Give the extent of all Plasmodium ovale-infected red blood cells.
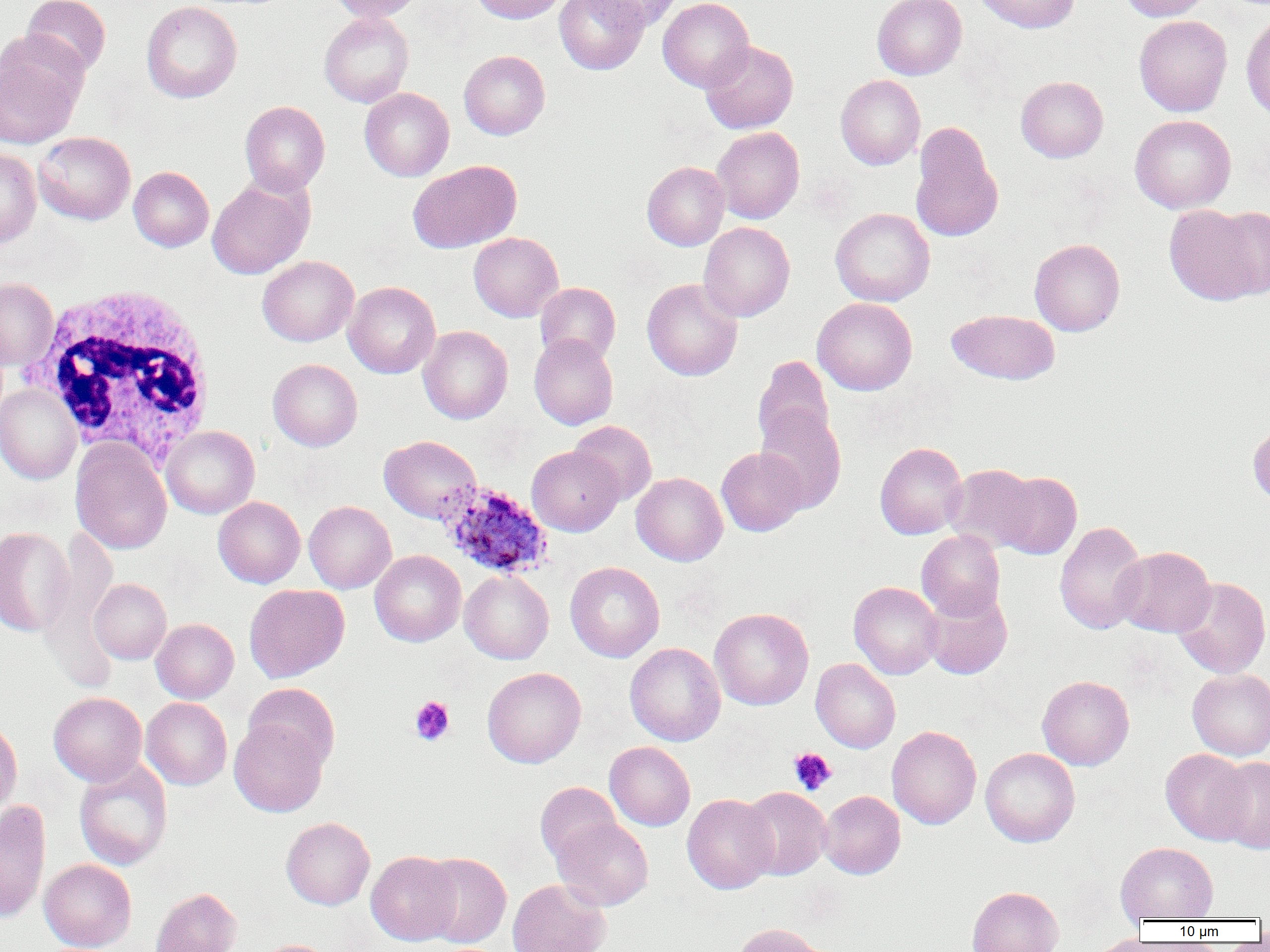

Approximate bounding boxes as named x1/y1/x2/y2 corners in pixels.
Plasmodium ovale-infected red blood cells: (x1=436, y1=482, x2=554, y2=579).

slide_level_diagnosis: Plasmodium ovale
uninfected_red_blood_cell_locations: 'approximate bounding boxes as named x1/y1/x2/y2 corners in pixels: (x1=21, y1=0, x2=111, y2=75), (x1=327, y1=0, x2=425, y2=22), (x1=469, y1=0, x2=566, y2=24), (x1=554, y1=0, x2=649, y2=74), (x1=588, y1=0, x2=682, y2=31), (x1=658, y1=0, x2=754, y2=92), (x1=872, y1=0, x2=966, y2=80), (x1=974, y1=0, x2=1079, y2=33), (x1=1119, y1=0, x2=1213, y2=21), (x1=141, y1=1, x2=242, y2=103), (x1=1241, y1=11, x2=1270, y2=121), (x1=319, y1=12, x2=414, y2=107), (x1=1134, y1=15, x2=1232, y2=116), (x1=0, y1=36, x2=87, y2=149), (x1=700, y1=40, x2=799, y2=134), (x1=459, y1=50, x2=550, y2=140), (x1=836, y1=74, x2=925, y2=170), (x1=1016, y1=76, x2=1108, y2=162), (x1=360, y1=87, x2=454, y2=181), (x1=240, y1=101, x2=330, y2=196), (x1=1129, y1=115, x2=1236, y2=214), (x1=910, y1=121, x2=1003, y2=243), (x1=712, y1=127, x2=804, y2=224), (x1=33, y1=131, x2=135, y2=225), (x1=0, y1=147, x2=41, y2=248), (x1=409, y1=160, x2=521, y2=253), (x1=642, y1=161, x2=730, y2=251), (x1=129, y1=166, x2=214, y2=252), (x1=207, y1=178, x2=313, y2=279), (x1=1165, y1=204, x2=1262, y2=305), (x1=830, y1=207, x2=935, y2=306), (x1=1211, y1=207, x2=1270, y2=299), (x1=698, y1=222, x2=795, y2=322), (x1=468, y1=232, x2=564, y2=322), (x1=1029, y1=238, x2=1125, y2=336), (x1=257, y1=256, x2=358, y2=346), (x1=0, y1=277, x2=58, y2=369), (x1=642, y1=278, x2=743, y2=381), (x1=344, y1=281, x2=440, y2=378), (x1=535, y1=282, x2=620, y2=365), (x1=812, y1=297, x2=917, y2=395), (x1=946, y1=309, x2=1059, y2=384), (x1=418, y1=326, x2=513, y2=424), (x1=529, y1=334, x2=618, y2=429), (x1=752, y1=356, x2=835, y2=454), (x1=268, y1=358, x2=362, y2=451), (x1=0, y1=384, x2=81, y2=485), (x1=754, y1=405, x2=846, y2=513), (x1=568, y1=420, x2=657, y2=505), (x1=1248, y1=422, x2=1270, y2=506), (x1=161, y1=426, x2=259, y2=518), (x1=379, y1=435, x2=481, y2=523), (x1=71, y1=438, x2=172, y2=555), (x1=875, y1=442, x2=968, y2=539), (x1=527, y1=446, x2=624, y2=536), (x1=716, y1=448, x2=808, y2=536), (x1=944, y1=464, x2=1039, y2=553), (x1=632, y1=472, x2=728, y2=566), (x1=995, y1=472, x2=1082, y2=560), (x1=213, y1=496, x2=305, y2=588), (x1=304, y1=500, x2=396, y2=593), (x1=1054, y1=520, x2=1148, y2=635), (x1=41, y1=526, x2=118, y2=648), (x1=0, y1=527, x2=74, y2=637), (x1=916, y1=530, x2=1005, y2=621), (x1=1112, y1=546, x2=1216, y2=637), (x1=370, y1=550, x2=466, y2=647), (x1=565, y1=561, x2=665, y2=662), (x1=459, y1=570, x2=554, y2=664), (x1=1173, y1=577, x2=1270, y2=678), (x1=89, y1=579, x2=171, y2=664), (x1=849, y1=581, x2=943, y2=679), (x1=244, y1=584, x2=349, y2=683), (x1=922, y1=589, x2=1012, y2=680), (x1=709, y1=607, x2=814, y2=710), (x1=151, y1=618, x2=239, y2=703), (x1=625, y1=642, x2=725, y2=746), (x1=811, y1=658, x2=901, y2=753), (x1=482, y1=666, x2=586, y2=768), (x1=1187, y1=669, x2=1270, y2=760), (x1=1037, y1=675, x2=1134, y2=770), (x1=243, y1=683, x2=340, y2=772), (x1=49, y1=692, x2=147, y2=786), (x1=141, y1=697, x2=232, y2=789), (x1=0, y1=718, x2=22, y2=819), (x1=229, y1=719, x2=328, y2=816), (x1=887, y1=726, x2=981, y2=829), (x1=605, y1=741, x2=695, y2=830), (x1=980, y1=747, x2=1079, y2=847), (x1=1160, y1=748, x2=1252, y2=844), (x1=1212, y1=756, x2=1270, y2=854), (x1=74, y1=758, x2=173, y2=871), (x1=535, y1=782, x2=622, y2=868), (x1=739, y1=787, x2=831, y2=880), (x1=818, y1=790, x2=905, y2=879), (x1=682, y1=793, x2=778, y2=894), (x1=0, y1=799, x2=50, y2=924), (x1=281, y1=817, x2=375, y2=910), (x1=552, y1=817, x2=654, y2=911), (x1=1115, y1=842, x2=1218, y2=922), (x1=366, y1=851, x2=461, y2=945), (x1=420, y1=853, x2=511, y2=948), (x1=39, y1=859, x2=136, y2=952), (x1=507, y1=879, x2=611, y2=952), (x1=966, y1=885, x2=1064, y2=952), (x1=150, y1=887, x2=242, y2=952), (x1=734, y1=923, x2=827, y2=952), (x1=1084, y1=935, x2=1157, y2=952), (x1=251, y1=939, x2=337, y2=952)'
white_blood_cell_locations: 'approximate bounding boxes as named x1/y1/x2/y2 corners in pixels: (x1=25, y1=283, x2=217, y2=466)'
magnification: 1000x
modality: light microscopy
preparation: thin blood smear
image_size: 1270×952 pixels
platelet_locations: 'approximate bounding boxes as named x1/y1/x2/y2 corners in pixels: (x1=409, y1=695, x2=455, y2=746), (x1=789, y1=747, x2=836, y2=795)'
field_of_view: single